Give the position of every malaria parasite.
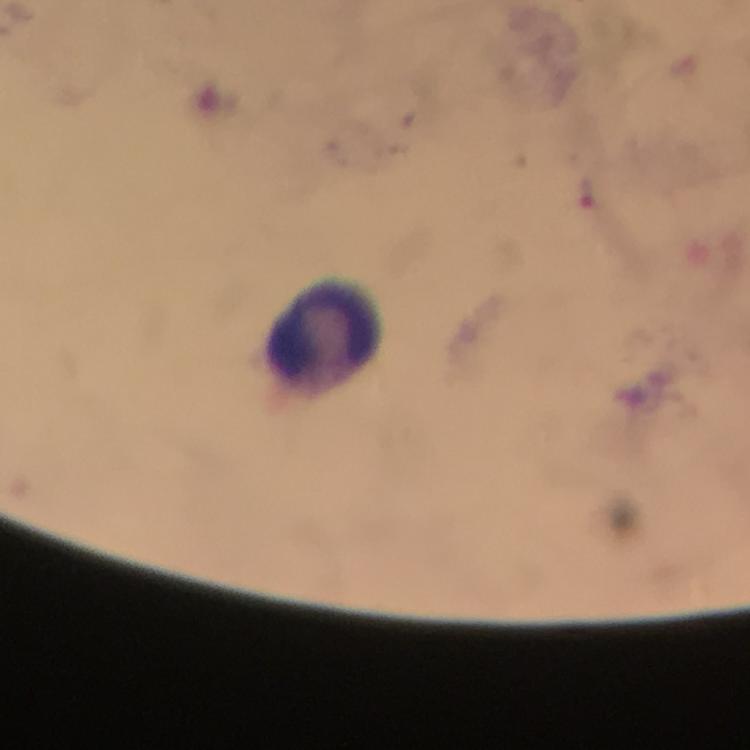

No malaria parasites seen.

Approximate object centers, in pixels from the top-left corner.
Summary:
  - Leukocyte locations: (x=325, y=333)
  - Image size: 750×750 pixels
  - Stain: Giemsa
  - Magnification: 100x
  - Preparation: thick blood smear
  - Capture: smartphone camera through the microscope
  - Immersion oil: applied
  - Context: from a malaria diagnostic workup
  - Cropped from: a single field of view